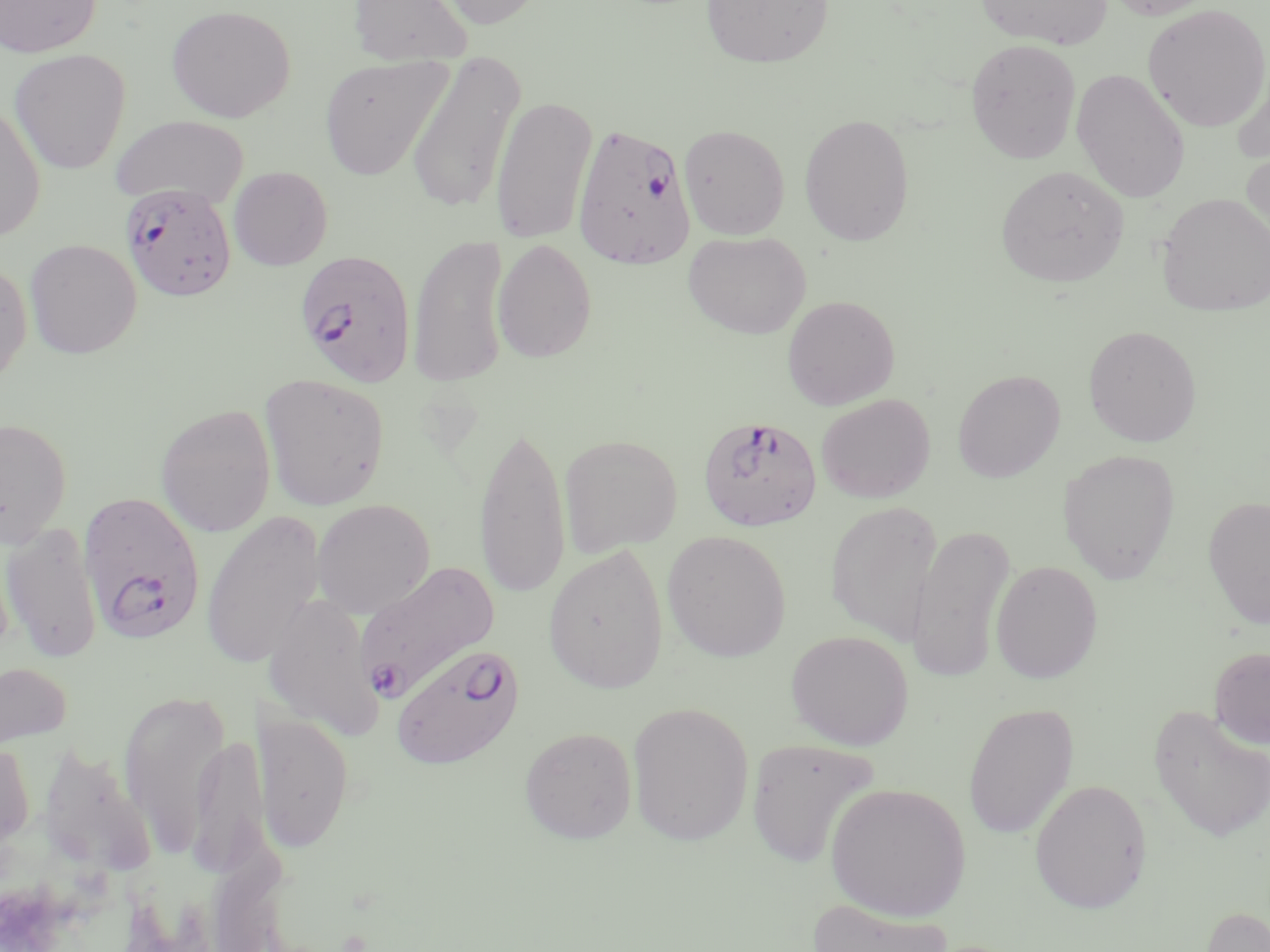

{
  "slide_level_diagnosis": "Plasmodium falciparum",
  "magnification": "1000x",
  "field_of_view": "single",
  "uninfected_red_blood_cell_locations": "approximate bounding boxes as [x1, y1, x2, y2] in pixels: [0, 0, 101, 58], [348, 0, 474, 66], [427, 0, 549, 29], [701, 0, 834, 68], [974, 0, 1114, 49], [1103, 0, 1221, 20], [166, 4, 296, 122], [1143, 4, 1270, 132], [965, 38, 1082, 164], [9, 49, 131, 174], [406, 52, 525, 215], [1231, 55, 1270, 165], [319, 56, 450, 179], [1071, 68, 1190, 203], [491, 96, 598, 245], [0, 102, 46, 241], [799, 113, 915, 245], [109, 115, 249, 210], [678, 123, 790, 239], [1240, 146, 1270, 263], [996, 164, 1129, 288], [228, 166, 333, 271], [1156, 193, 1270, 317], [683, 230, 812, 339], [408, 234, 511, 388], [24, 238, 142, 359], [492, 238, 597, 363], [0, 257, 32, 387], [781, 295, 900, 410], [1083, 325, 1202, 447], [952, 369, 1065, 483], [259, 372, 390, 511], [816, 393, 935, 503], [156, 403, 276, 537], [0, 417, 72, 547], [473, 422, 572, 602], [558, 433, 683, 557], [1058, 448, 1182, 583], [1202, 494, 1270, 630], [312, 499, 435, 619], [825, 501, 943, 644], [201, 511, 325, 669], [1, 522, 103, 664], [908, 525, 1015, 684], [662, 530, 791, 662], [543, 544, 669, 694], [990, 560, 1103, 683], [263, 592, 383, 741], [786, 629, 914, 750], [1209, 646, 1270, 749], [0, 660, 72, 753], [118, 688, 231, 857], [627, 701, 754, 846], [963, 703, 1079, 840], [1148, 705, 1270, 843], [252, 709, 355, 854], [519, 726, 637, 844], [190, 730, 269, 877], [0, 736, 35, 861], [746, 738, 880, 869], [1030, 778, 1151, 914], [826, 782, 971, 921], [807, 898, 954, 952], [1198, 905, 1270, 952]",
  "plasmodium_falciparum_infected_red_blood_cell_locations": "approximate bounding boxes as [x1, y1, x2, y2] in pixels: [572, 121, 696, 270], [115, 180, 240, 302], [294, 249, 416, 387], [697, 414, 823, 532], [77, 491, 205, 644], [354, 561, 500, 701], [390, 641, 526, 771]",
  "stain": "May-Grünwald-Giemsa",
  "preparation": "thin blood smear",
  "image_size": "1270×952 pixels",
  "modality": "light microscopy"
}